Evaluate for malaria.
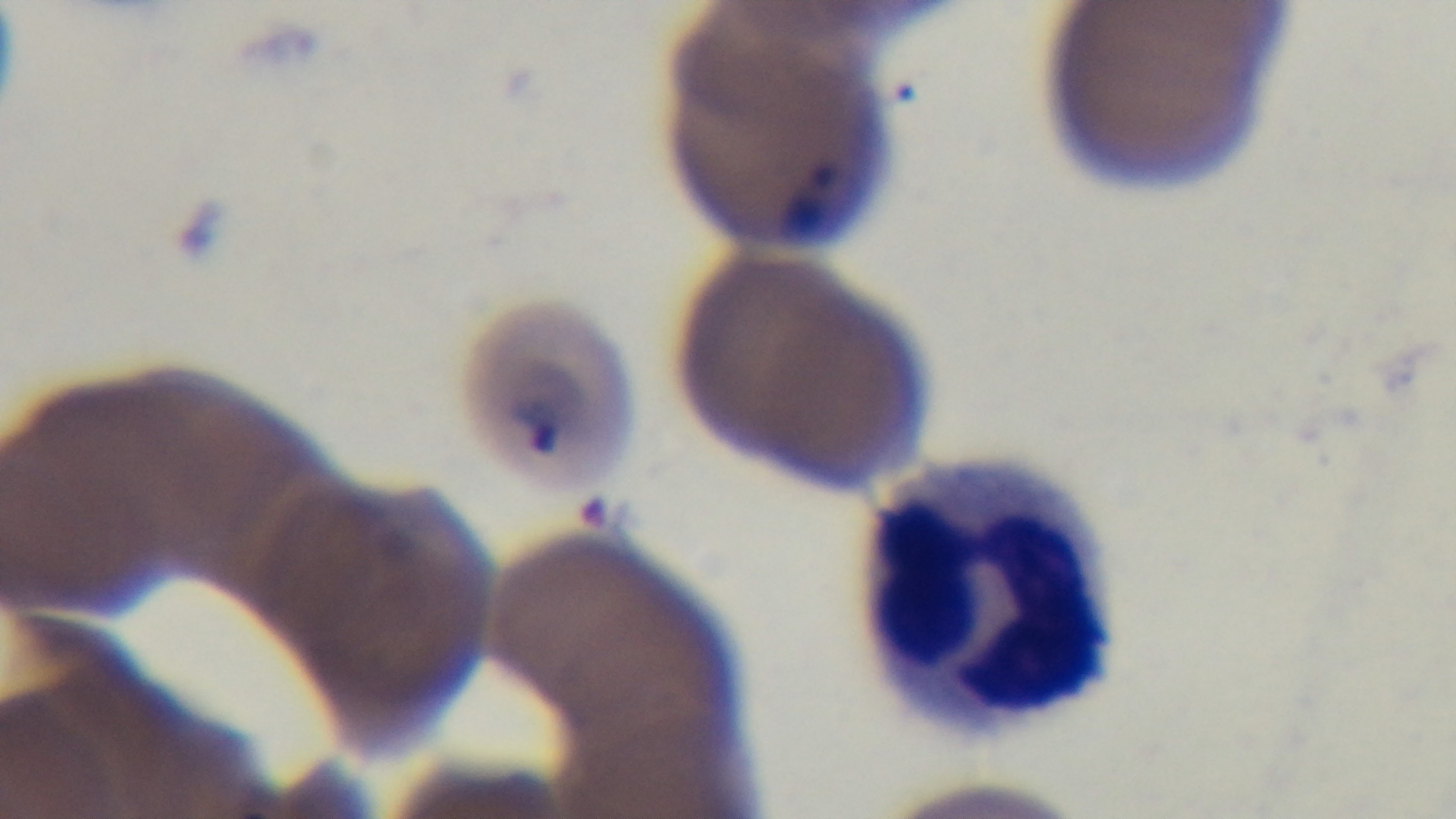

Infected.

stain = Giemsa
capture = mounted 4K digital camera
field of view = single
objective = 100x oil immersion
preparation = thin blood film
modality = light microscopy